Assess this cell for malaria.
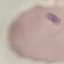

Parasitized.

Giemsa-stained preparation. Automatically extracted cell patch, resized to 64 × 64 pixels. Thin blood film. Acquired by smartphone through the microscope eyepiece.